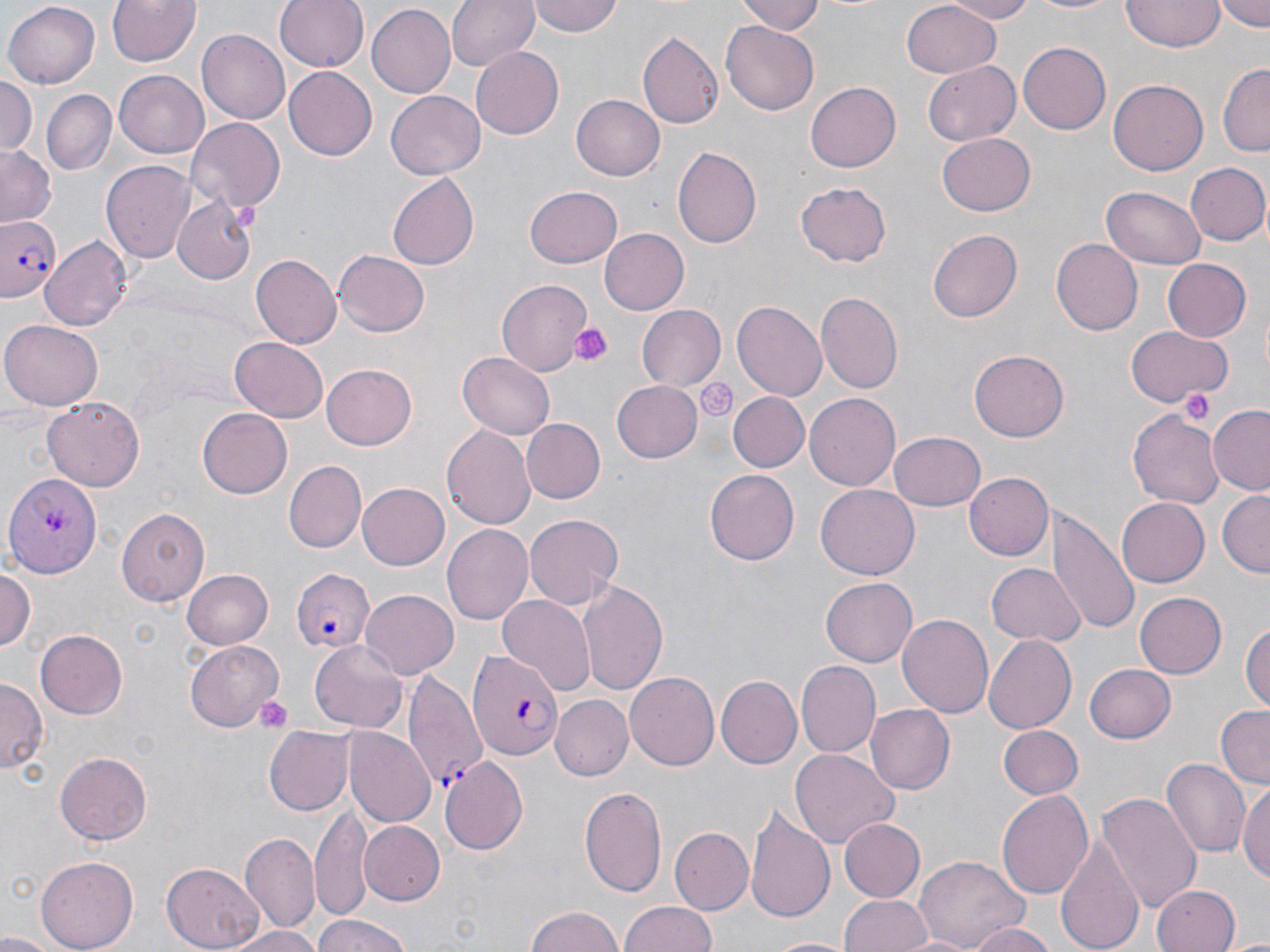

Summary:
  - Coordinate format: approximate bounding boxes as [x1, y1, x2, y2] in pixels
  - Uninfected red blood cell locations: [104, 0, 201, 69], [275, 0, 370, 72], [447, 0, 538, 71], [528, 0, 624, 39], [740, 0, 829, 35], [941, 0, 1041, 23], [1021, 0, 1126, 16], [1215, 0, 1270, 29], [1122, 1, 1226, 53], [3, 2, 101, 88], [899, 2, 1002, 78], [367, 3, 457, 98], [720, 22, 820, 114], [197, 29, 290, 125], [638, 32, 723, 128], [1020, 40, 1112, 135], [469, 46, 563, 140], [924, 61, 1021, 146], [1217, 62, 1270, 155], [283, 66, 376, 160], [115, 71, 208, 160], [0, 76, 35, 157], [1109, 80, 1208, 175], [805, 81, 900, 173], [43, 92, 114, 173], [387, 92, 485, 179], [572, 94, 667, 180], [186, 118, 287, 214], [936, 132, 1036, 216], [0, 146, 55, 228], [673, 147, 761, 247], [101, 160, 196, 265], [1185, 162, 1270, 246], [388, 172, 480, 269], [796, 183, 892, 266], [525, 185, 623, 268], [1102, 186, 1205, 268], [610, 192, 720, 307], [171, 196, 258, 284], [929, 227, 1023, 323], [597, 228, 688, 314], [40, 234, 132, 329], [1052, 238, 1143, 335], [333, 249, 429, 338], [250, 255, 340, 348], [1162, 258, 1251, 340], [498, 279, 593, 375], [818, 292, 904, 391], [733, 302, 826, 400], [637, 305, 726, 390], [1, 319, 104, 410], [1124, 325, 1232, 405], [230, 336, 327, 419], [970, 350, 1070, 441], [458, 352, 554, 439], [322, 363, 418, 449], [610, 380, 703, 463], [728, 391, 809, 472], [804, 393, 901, 491], [41, 396, 147, 493], [1209, 406, 1270, 496], [197, 407, 293, 499], [1128, 412, 1222, 506], [520, 418, 605, 504], [442, 425, 535, 529], [890, 431, 986, 511], [282, 461, 365, 552], [705, 469, 799, 566], [5, 472, 101, 577], [964, 472, 1053, 561], [358, 481, 451, 569], [816, 485, 918, 579], [1216, 490, 1269, 577], [1118, 498, 1210, 586], [115, 507, 208, 607], [1046, 507, 1137, 636], [524, 513, 623, 608], [443, 524, 531, 625], [988, 562, 1082, 647], [0, 566, 36, 654], [182, 569, 274, 649], [580, 577, 668, 696], [821, 577, 917, 667], [358, 589, 458, 680], [1134, 591, 1227, 679], [497, 594, 596, 702], [896, 612, 993, 715], [1242, 616, 1270, 717], [37, 628, 130, 717], [983, 634, 1076, 733], [184, 639, 282, 730], [310, 640, 406, 731], [795, 661, 880, 758], [1086, 665, 1177, 743], [626, 672, 719, 772], [716, 675, 802, 768], [0, 680, 44, 774], [553, 696, 631, 780], [865, 704, 954, 793], [1215, 705, 1270, 790], [263, 725, 354, 816], [997, 725, 1082, 800], [345, 727, 435, 827], [790, 749, 898, 846], [55, 750, 152, 844], [439, 757, 529, 857], [1162, 757, 1251, 856], [1238, 780, 1270, 886], [581, 785, 667, 896], [996, 789, 1093, 899], [1099, 792, 1201, 916], [312, 806, 373, 924], [745, 806, 836, 925], [838, 817, 924, 901], [361, 821, 444, 905], [668, 827, 752, 916], [1058, 831, 1145, 952], [240, 835, 318, 933], [912, 853, 1031, 952], [34, 856, 138, 951], [161, 864, 265, 950], [1153, 884, 1241, 952], [839, 894, 933, 952], [619, 901, 720, 952], [524, 905, 628, 952], [306, 914, 415, 952], [965, 920, 1057, 951], [223, 926, 326, 952], [0, 932, 61, 952], [1227, 934, 1270, 952], [764, 935, 852, 952]
  - Platelet locations: [570, 321, 612, 367], [696, 378, 738, 422], [1180, 389, 1216, 423], [255, 696, 292, 732]
  - Plasmodium falciparum-infected red blood cell locations: [1, 215, 65, 301], [292, 568, 372, 653], [467, 648, 563, 762], [402, 670, 487, 791]
  - Slide-level diagnosis: Plasmodium falciparum
  - Preparation: thin blood smear
  - Stain: May-Grünwald-Giemsa
  - Field of view: single
  - Magnification: 1000x
  - Image size: 1270×952 pixels
  - Modality: optical microscopy